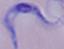
magnification: 1000x
modality: photomicrograph
identification: trypanosome